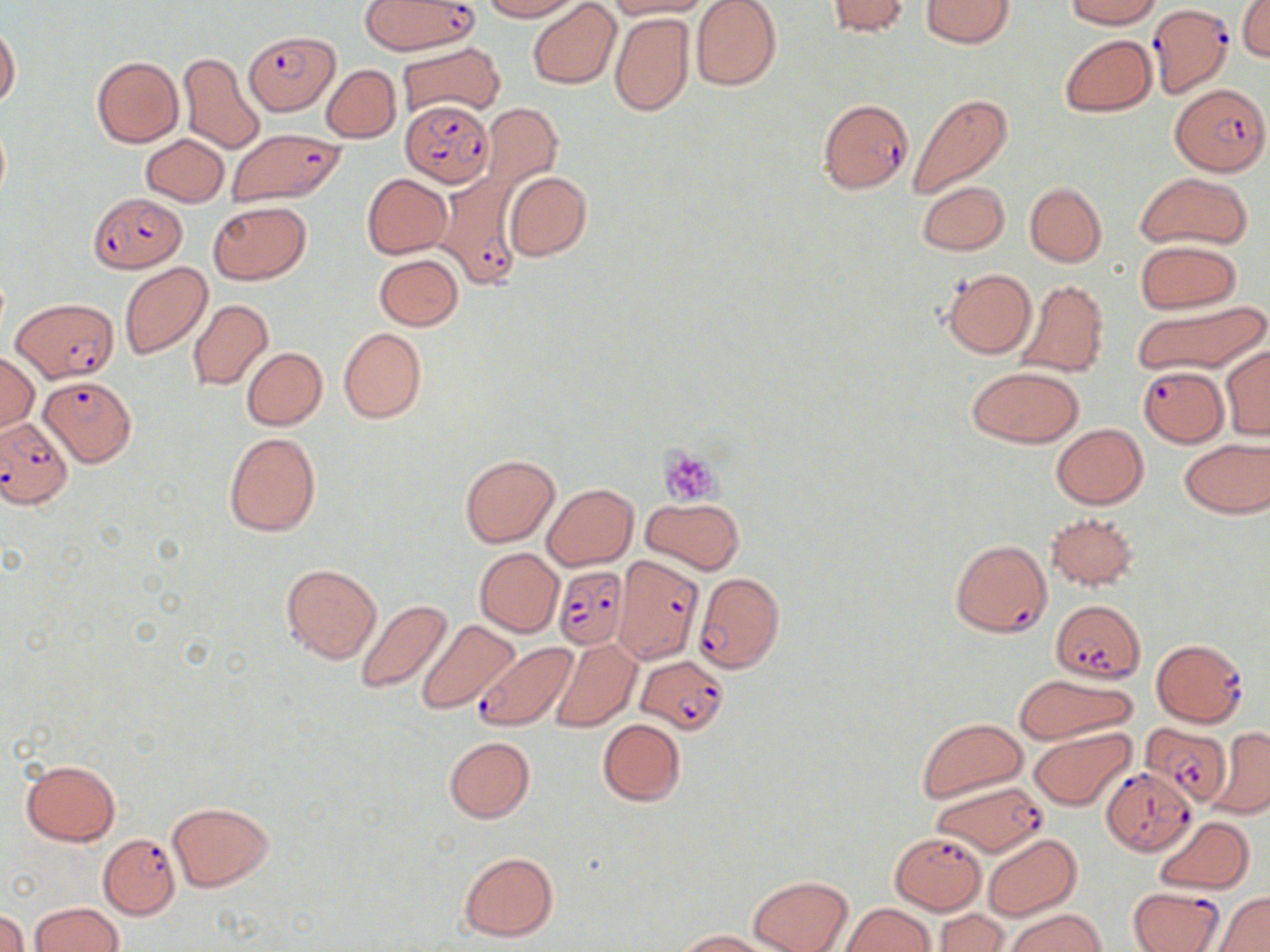
slide_level_diagnosis: Plasmodium falciparum
magnification: 1000x
platelet_locations: 'approximate bounding boxes as named x1/y1/x2/y2 corners in pixels: (x1=660, y1=447, x2=718, y2=503)'
plasmodium_falciparum_infected_red_blood_cell_locations: 'approximate bounding boxes as named x1/y1/x2/y2 corners in pixels: (x1=358, y1=0, x2=475, y2=55), (x1=1147, y1=6, x2=1234, y2=98), (x1=244, y1=28, x2=339, y2=119), (x1=1171, y1=84, x2=1267, y2=178), (x1=818, y1=98, x2=913, y2=192), (x1=400, y1=102, x2=494, y2=187), (x1=224, y1=128, x2=346, y2=209), (x1=436, y1=172, x2=526, y2=287), (x1=88, y1=193, x2=184, y2=272), (x1=12, y1=297, x2=119, y2=382), (x1=1135, y1=365, x2=1230, y2=446), (x1=37, y1=376, x2=133, y2=468), (x1=0, y1=416, x2=73, y2=509), (x1=950, y1=538, x2=1052, y2=638), (x1=613, y1=557, x2=703, y2=663), (x1=555, y1=565, x2=629, y2=651), (x1=693, y1=571, x2=785, y2=673), (x1=1051, y1=600, x2=1145, y2=683), (x1=1151, y1=638, x2=1249, y2=728), (x1=473, y1=643, x2=575, y2=731), (x1=635, y1=656, x2=729, y2=735), (x1=1141, y1=722, x2=1231, y2=807), (x1=1101, y1=767, x2=1195, y2=855), (x1=930, y1=780, x2=1046, y2=858), (x1=97, y1=833, x2=181, y2=919), (x1=891, y1=833, x2=986, y2=913), (x1=1128, y1=886, x2=1225, y2=952)'
image_size: 1270×952 pixels
stain: May-Grünwald-Giemsa
uninfected_red_blood_cell_locations: 'approximate bounding boxes as named x1/y1/x2/y2 corners in pixels: (x1=480, y1=0, x2=581, y2=21), (x1=528, y1=0, x2=620, y2=89), (x1=606, y1=0, x2=713, y2=18), (x1=691, y1=0, x2=781, y2=90), (x1=824, y1=0, x2=912, y2=38), (x1=919, y1=0, x2=1017, y2=48), (x1=1063, y1=0, x2=1164, y2=28), (x1=1238, y1=1, x2=1270, y2=62), (x1=609, y1=12, x2=694, y2=116), (x1=0, y1=24, x2=20, y2=109), (x1=1060, y1=35, x2=1157, y2=117), (x1=397, y1=41, x2=505, y2=120), (x1=177, y1=52, x2=265, y2=154), (x1=91, y1=55, x2=183, y2=148), (x1=321, y1=64, x2=401, y2=143), (x1=907, y1=93, x2=1013, y2=199), (x1=479, y1=100, x2=563, y2=199), (x1=0, y1=123, x2=10, y2=201), (x1=141, y1=134, x2=229, y2=206), (x1=1137, y1=171, x2=1253, y2=251), (x1=503, y1=172, x2=592, y2=261), (x1=361, y1=173, x2=452, y2=259), (x1=917, y1=181, x2=1008, y2=255), (x1=1024, y1=183, x2=1106, y2=266), (x1=208, y1=201, x2=311, y2=285), (x1=1135, y1=240, x2=1241, y2=313), (x1=374, y1=253, x2=464, y2=330), (x1=120, y1=263, x2=212, y2=359), (x1=941, y1=268, x2=1037, y2=358), (x1=1014, y1=278, x2=1108, y2=378), (x1=187, y1=299, x2=273, y2=391), (x1=1130, y1=300, x2=1268, y2=376), (x1=339, y1=328, x2=427, y2=424), (x1=1221, y1=344, x2=1270, y2=439), (x1=242, y1=347, x2=327, y2=431), (x1=0, y1=352, x2=40, y2=431), (x1=965, y1=365, x2=1084, y2=448), (x1=1051, y1=424, x2=1148, y2=509), (x1=223, y1=431, x2=322, y2=537), (x1=1179, y1=439, x2=1270, y2=517), (x1=460, y1=455, x2=559, y2=547), (x1=542, y1=482, x2=639, y2=572), (x1=641, y1=497, x2=743, y2=574), (x1=1045, y1=511, x2=1139, y2=590), (x1=474, y1=548, x2=563, y2=636), (x1=280, y1=562, x2=381, y2=664), (x1=356, y1=599, x2=455, y2=694), (x1=417, y1=621, x2=521, y2=715), (x1=551, y1=639, x2=641, y2=733), (x1=1012, y1=674, x2=1138, y2=745), (x1=596, y1=718, x2=685, y2=806), (x1=918, y1=718, x2=1028, y2=801), (x1=1209, y1=726, x2=1270, y2=819), (x1=1028, y1=729, x2=1135, y2=811), (x1=444, y1=736, x2=535, y2=822), (x1=20, y1=758, x2=121, y2=847), (x1=166, y1=801, x2=274, y2=892), (x1=1154, y1=817, x2=1255, y2=894), (x1=983, y1=834, x2=1082, y2=920), (x1=459, y1=851, x2=558, y2=941), (x1=747, y1=875, x2=853, y2=952), (x1=1213, y1=890, x2=1270, y2=951), (x1=841, y1=902, x2=936, y2=952), (x1=28, y1=903, x2=123, y2=952), (x1=0, y1=909, x2=28, y2=952), (x1=1005, y1=909, x2=1105, y2=952), (x1=934, y1=910, x2=1008, y2=952), (x1=674, y1=929, x2=774, y2=951)'
modality: optical microscopy
field_of_view: single
preparation: thin blood smear